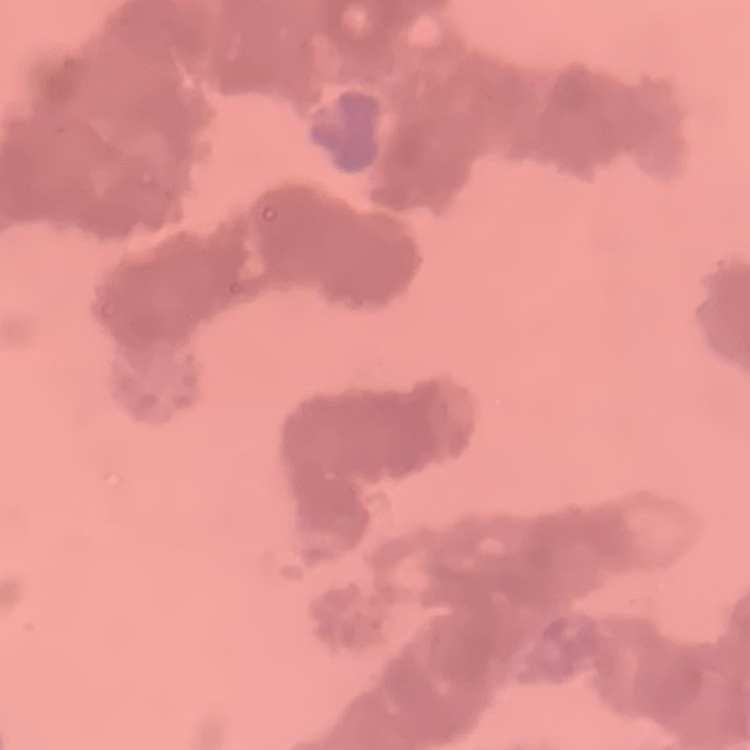
The erythrocytes show rouleaux formation. Stained with either Field's or Giemsa. Thin blood film. Square crop of a larger photomicrograph.